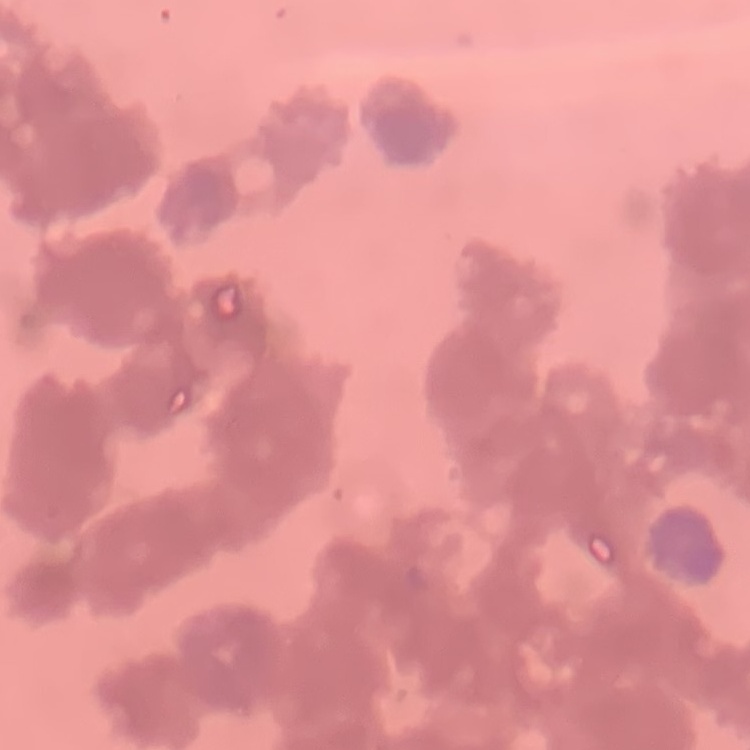
erythrocyte morphology = rouleaux formation
preparation = thin blood smear
stain = Field's or Giemsa
image type = one tile cut from a larger photomicrograph